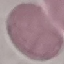

Malaria status: uninfected. Photographed with a smartphone camera at the microscope eyepiece. Thin blood smear. Cell patch, automatically extracted from a larger field of view and resized to 64 × 64 pixels. Giemsa-stained preparation.